Assess the morphology of the erythrocytes.
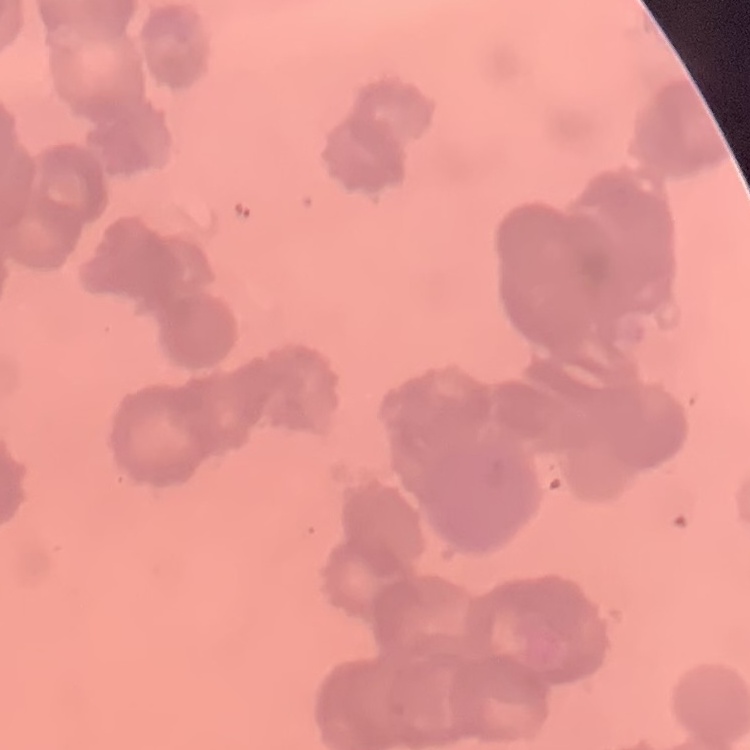

Rouleaux formation.

One tile cut from a larger photomicrograph. Stained with either Field's or Giemsa. Thin blood film.